State which parasite is depicted.
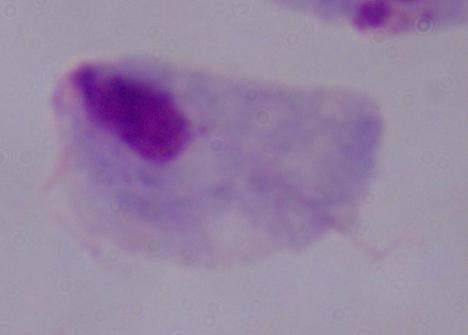

This is a trichomonad.

Summary:
  - Modality: photomicrograph
  - Magnification: 1000x